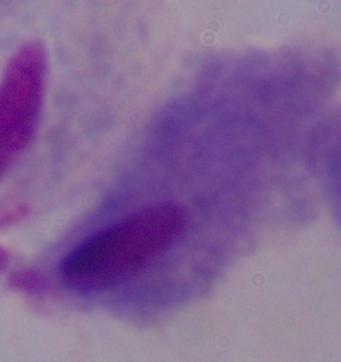
modality = micrograph
magnification = 1000x
identification = trichomonad